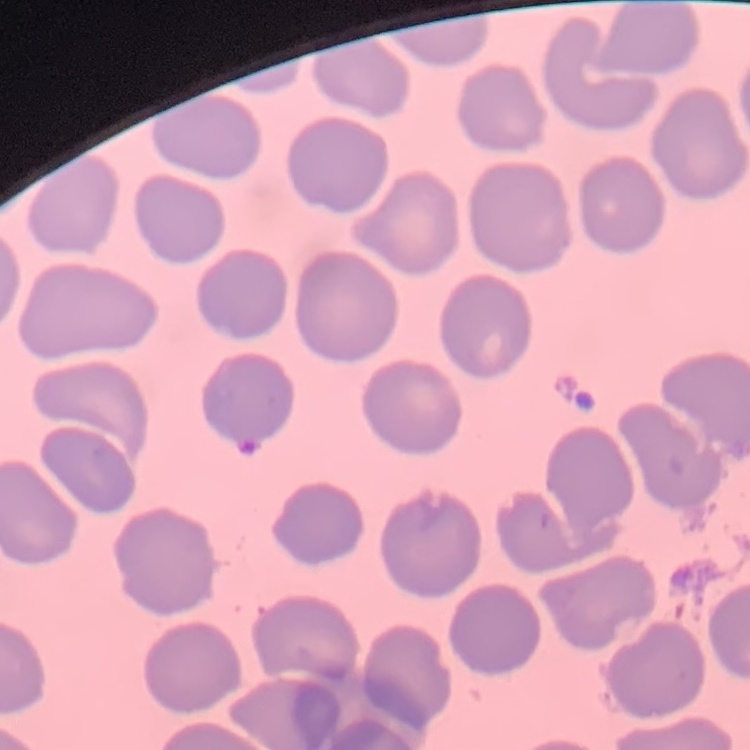

Summary:
  - Erythrocyte morphology: no rouleaux formation
  - Image type: square crop of a larger photomicrograph
  - Stain: Field's or Giemsa
  - Preparation: thin blood film